Classify this cell by malaria status.
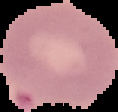
It is uninfected.

image type = segmented cell region on a black background
preparation = thin blood film
image size = 118×112 pixels